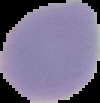

From a thin blood smear. Result: no malaria parasites detected. Image is 100×103 pixels. Segmented cell region on a black background.